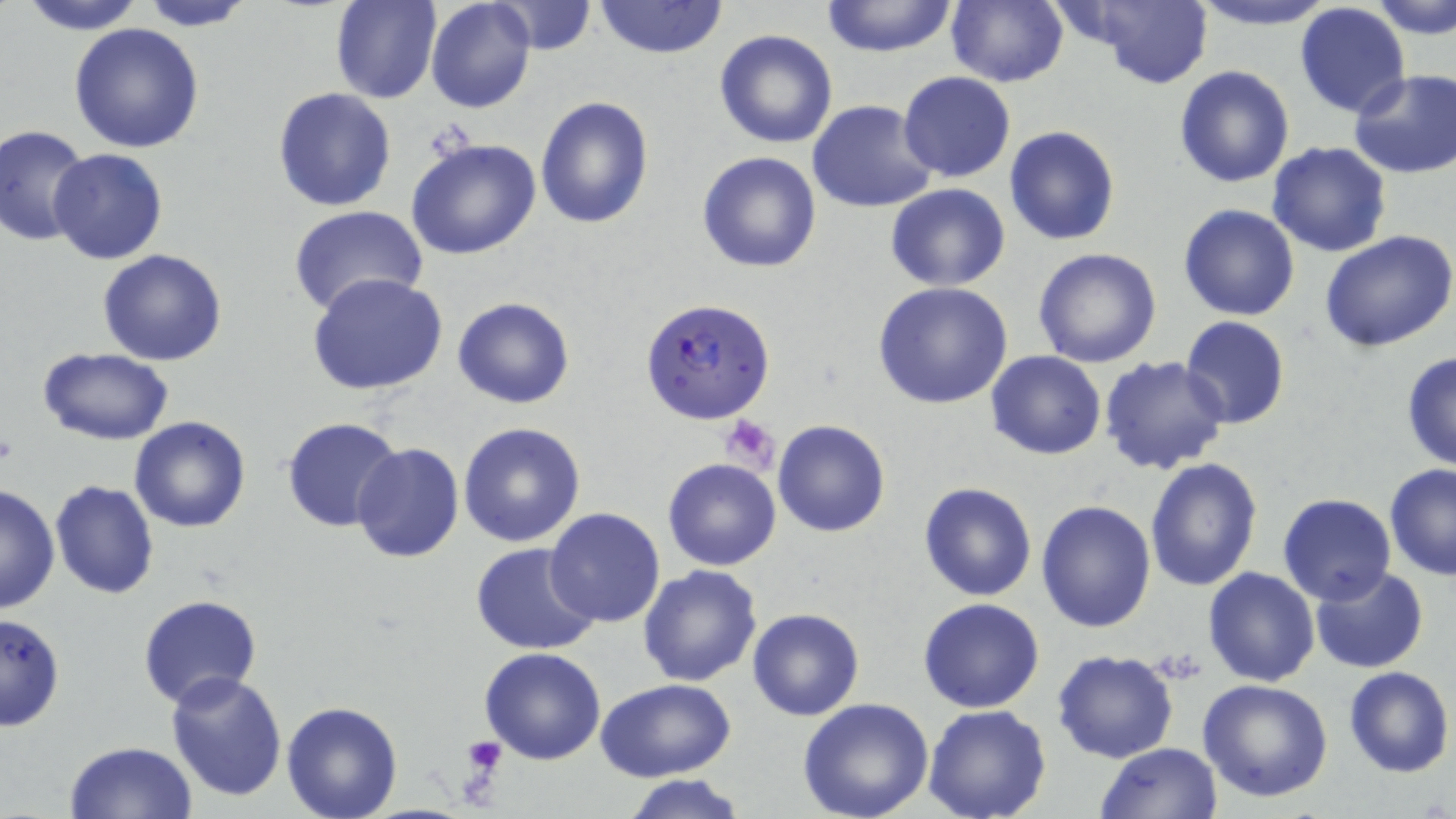
slide-level diagnosis = Plasmodium falciparum
magnification = 1000x
field of view = single
stain = May-Grünwald-Giemsa
uninfected red blood cell locations = approximate bounding boxes as (x1, y1, x2, y2) in pixels: (15, 0, 149, 35), (426, 0, 536, 114), (945, 0, 1069, 87), (1186, 0, 1338, 30), (136, 1, 255, 30), (329, 1, 442, 104), (819, 1, 961, 57), (1372, 1, 1456, 40), (491, 2, 597, 54), (592, 2, 729, 59), (1065, 2, 1217, 86), (1295, 4, 1410, 117), (68, 23, 205, 154), (713, 29, 838, 149), (1174, 65, 1295, 187), (1347, 67, 1456, 177), (898, 71, 1015, 182), (273, 88, 397, 211), (535, 95, 654, 229), (806, 99, 938, 212), (1005, 126, 1120, 245), (1, 127, 91, 247), (406, 137, 542, 260), (1267, 142, 1393, 257), (46, 148, 167, 265), (697, 151, 823, 273), (885, 184, 1012, 292), (1177, 203, 1299, 323), (287, 205, 427, 318), (1320, 230, 1456, 353), (98, 248, 228, 366), (1033, 248, 1163, 368), (307, 273, 448, 396), (874, 282, 1014, 409), (452, 296, 575, 408), (1180, 316, 1290, 428), (37, 346, 176, 446), (987, 351, 1106, 459), (1400, 351, 1456, 473), (1099, 355, 1232, 476), (129, 416, 251, 532), (281, 417, 403, 533), (773, 419, 890, 537), (458, 422, 586, 547), (352, 443, 464, 563), (1146, 456, 1262, 592), (662, 458, 780, 570), (1384, 463, 1456, 580), (50, 481, 160, 600), (918, 482, 1038, 602), (0, 483, 59, 616), (1278, 494, 1397, 606), (1037, 499, 1157, 632), (544, 507, 667, 628), (470, 541, 600, 655), (638, 564, 763, 686), (1310, 565, 1429, 674), (1202, 566, 1320, 687), (138, 595, 263, 711), (917, 599, 1044, 714), (747, 608, 865, 722), (0, 613, 66, 733), (478, 646, 607, 765), (1050, 649, 1178, 763), (1342, 667, 1453, 778), (166, 670, 289, 801), (598, 679, 735, 783), (1197, 679, 1333, 804), (796, 699, 936, 819), (280, 701, 404, 818), (923, 704, 1052, 819), (63, 741, 198, 819), (1097, 742, 1224, 819), (621, 774, 748, 819)
Plasmodium falciparum-infected red blood cell locations = approximate bounding boxes as (x1, y1, x2, y2) in pixels: (642, 299, 776, 424)
platelet locations = approximate bounding boxes as (x1, y1, x2, y2) in pixels: (720, 416, 780, 472), (464, 737, 507, 777)
preparation = thin blood film
modality = optical microscopy
image size = 1456×819 pixels